Report the malaria status of this cell.
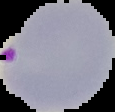

Parasitized.

image type = cell region segmented out of the field of view; surrounding area masked to black
preparation = thin blood smear
image size = 115×112 pixels